Identify the cell.
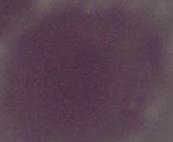

An erythrocyte.

Micrograph. 1000x magnification.